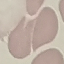 Malaria status: uninfected. Cell patch, automatically extracted from a larger field of view and resized to 64 × 64 pixels. Giemsa-stained preparation. Acquired by smartphone through the microscope eyepiece. Thin smear of blood.